Give the position of every leukocyte visible.
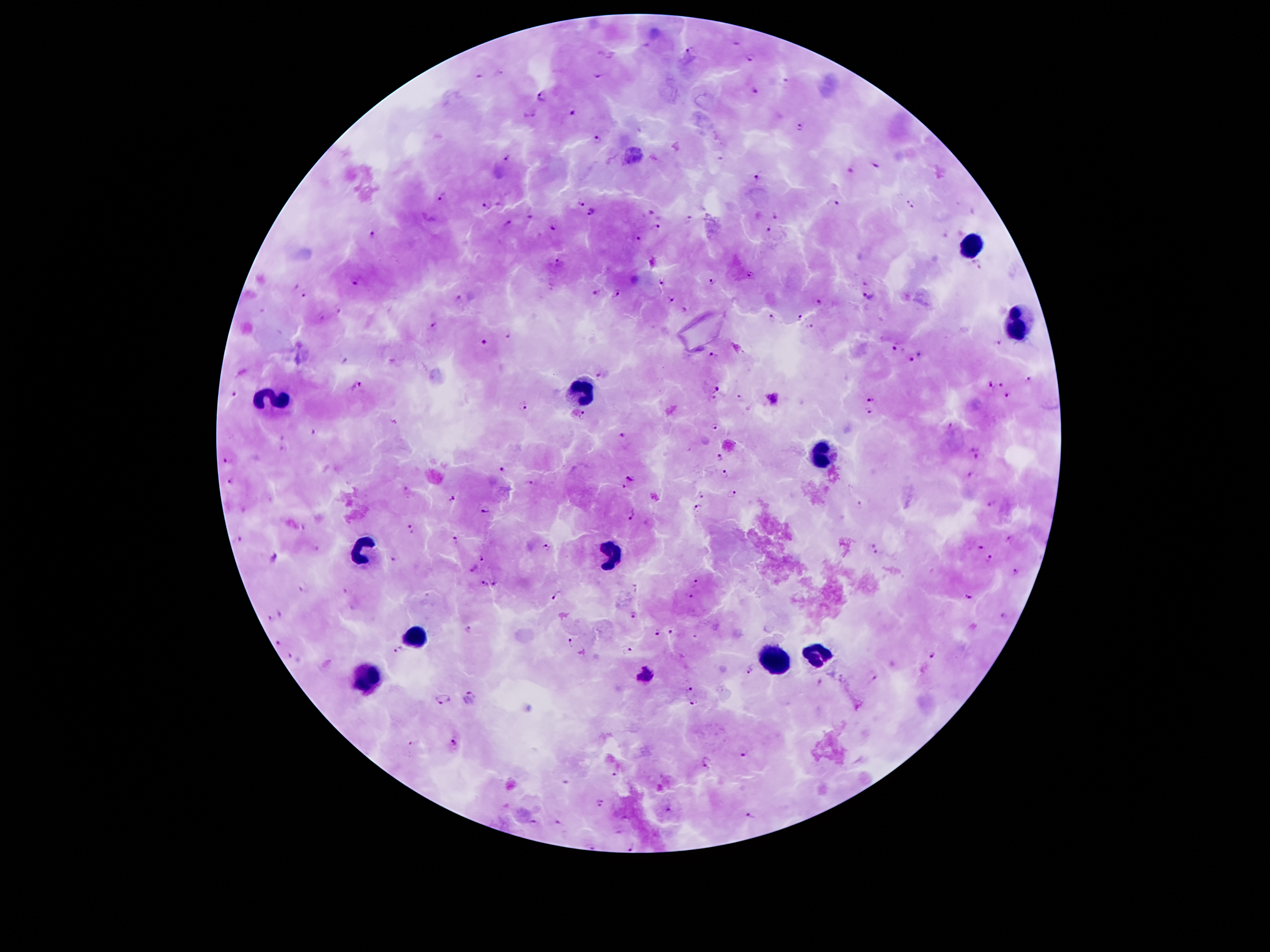
Approximate centers as (x, y) in pixels.
Leukocytes: (971, 245), (1017, 325), (585, 392), (272, 402), (826, 457), (366, 549), (612, 556), (414, 637), (818, 652), (776, 656), (366, 684).

Plasmodium parasite locations = (736, 43), (646, 45), (690, 50), (750, 56), (479, 73), (598, 74), (785, 80), (754, 90), (543, 96), (532, 112), (572, 112), (799, 127), (598, 138), (634, 155), (508, 158), (876, 164), (850, 169), (757, 177), (444, 196), (834, 202), (581, 203), (487, 204), (911, 204), (651, 211), (592, 212), (530, 214), (775, 215), (688, 219), (506, 224), (656, 226), (552, 227), (766, 230), (373, 235), (945, 235), (635, 238), (559, 261), (975, 261), (980, 268), (750, 272), (713, 280), (356, 281), (661, 282), (865, 283), (595, 292), (303, 293), (616, 294), (869, 296), (459, 298), (671, 298), (820, 302), (341, 310), (684, 310), (798, 316), (322, 317), (771, 317), (434, 324), (809, 326), (509, 336), (482, 342), (1000, 344), (894, 348), (713, 355), (919, 355), (910, 358), (345, 361), (598, 374), (1029, 380), (990, 383), (1002, 383), (357, 385), (716, 388), (233, 394), (1008, 395), (738, 398), (711, 399), (774, 399), (869, 399), (523, 407), (869, 412), (582, 415), (715, 425), (952, 426), (313, 432), (624, 435), (279, 436), (283, 448), (972, 448), (719, 455), (976, 457), (227, 460), (501, 470), (726, 475), (969, 475), (630, 479), (229, 480), (530, 484), (621, 487), (405, 490), (702, 495), (733, 495), (452, 498), (859, 503), (993, 504), (698, 508), (485, 511), (632, 515), (412, 529), (456, 539), (1011, 540), (238, 541), (871, 543), (547, 547), (316, 548), (980, 548), (876, 551), (272, 557), (481, 557), (391, 558), (990, 559), (475, 568), (1015, 572), (696, 581), (497, 582), (485, 583), (305, 587), (690, 595), (556, 596), (969, 598), (280, 613), (634, 615), (1003, 616), (271, 617), (469, 630), (658, 631), (671, 632), (695, 637), (569, 642), (277, 643), (628, 648), (397, 649), (290, 655), (934, 656), (750, 669), (646, 676), (872, 676), (820, 681), (688, 689), (471, 695), (443, 699), (691, 703), (413, 743), (454, 743), (743, 755), (708, 762), (615, 774), (599, 802), (670, 809), (749, 815), (624, 819), (559, 820), (533, 822), (593, 846), (633, 846)
stain = Giemsa
preparation = thick blood film
image size = 1270×952 pixels
capture = smartphone through the microscope eyepiece
patient malaria status = positive for Plasmodium falciparum
magnification = 100x
field of view = single